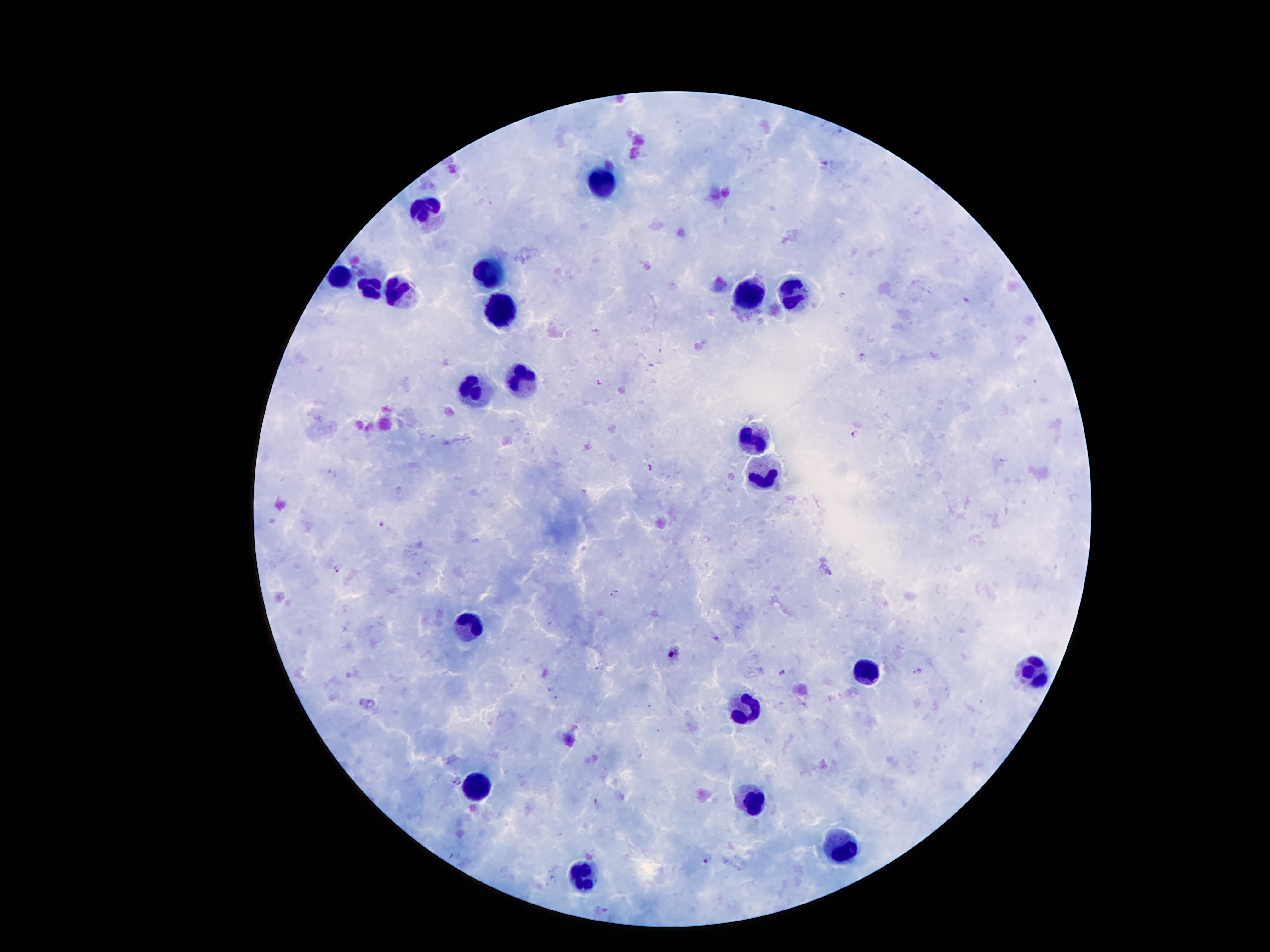

patient_malaria_status: infected with Plasmodium falciparum
capture: smartphone camera through the microscope eyepiece
field_of_view: one from this slide
stain: Giemsa
preparation: thick peripheral-blood smear
malaria_parasite_locations: 'approximate object centers, in pixels from the top-left corner: (x=825, y=166), (x=842, y=296), (x=966, y=298), (x=597, y=331), (x=863, y=352), (x=598, y=382), (x=855, y=432), (x=432, y=437), (x=649, y=466), (x=331, y=471), (x=380, y=523), (x=336, y=568), (x=616, y=590), (x=611, y=596), (x=781, y=671), (x=918, y=671), (x=551, y=688), (x=555, y=698), (x=651, y=707), (x=706, y=861)'
magnification: 100x
image_size: 1270×952 pixels
leukocyte_locations: 'approximate object centers, in pixels from the top-left corner: (x=603, y=180), (x=427, y=206), (x=494, y=272), (x=337, y=278), (x=368, y=289), (x=796, y=289), (x=404, y=295), (x=740, y=295), (x=502, y=310), (x=522, y=383), (x=469, y=391), (x=754, y=439), (x=752, y=468), (x=469, y=626), (x=1034, y=670), (x=866, y=671), (x=740, y=710), (x=474, y=786), (x=749, y=796), (x=841, y=849), (x=578, y=878)'